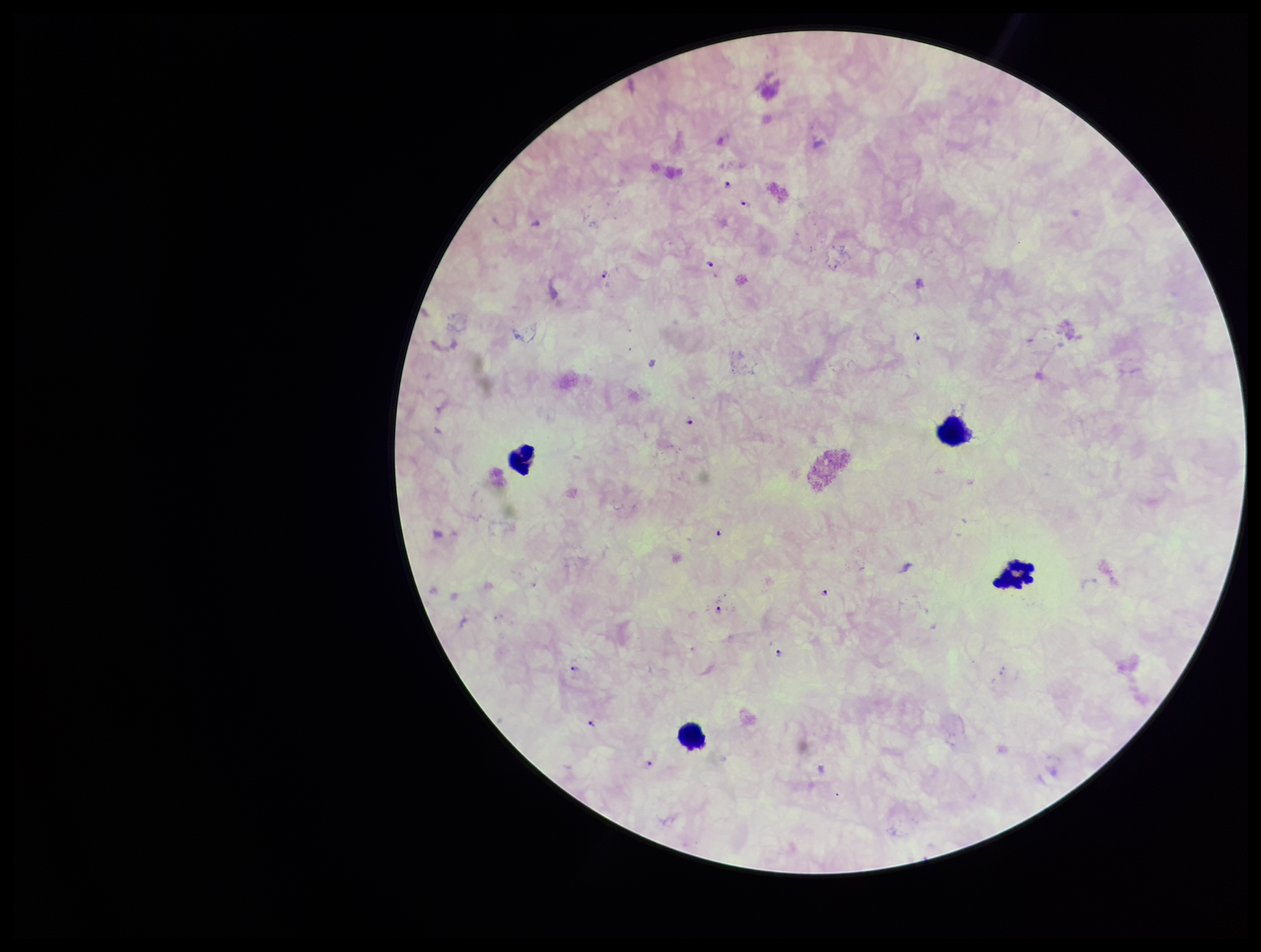

Plasmodium parasites: identified. One field from this slide. Species reported for this patient: Plasmodium falciparum. Parasite count: 16. Preparation: thick. Patient malaria status: positive. Image is 1261×952 pixels. Leukocyte count: 4. Photographed through the microscope eyepiece with a smartphone camera. Stained with Giemsa.